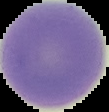

preparation = thin blood film
result = negative for Plasmodium parasites
image type = segmented cell region with the area outside set to black
image size = 109×112 pixels